Name the blood parasite species.
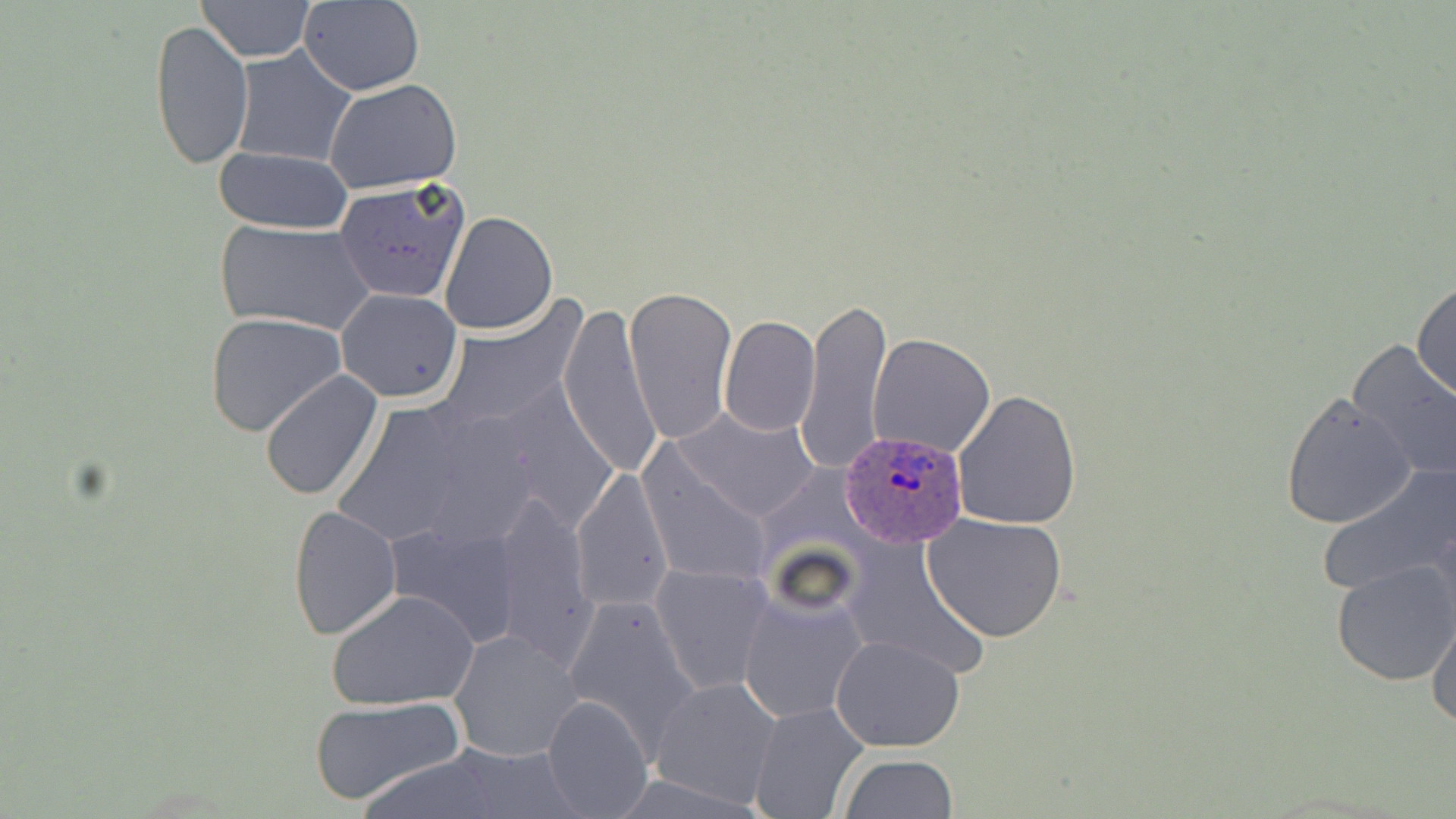

Plasmodium ovale.

Summary:
  - Coordinate format: approximate bounding boxes as named x1/y1/x2/y2 corners in pixels
  - Uninfected red blood cell locations: (x1=195, y1=0, x2=315, y2=61), (x1=298, y1=0, x2=423, y2=95), (x1=150, y1=18, x2=253, y2=171), (x1=231, y1=47, x2=357, y2=167), (x1=323, y1=78, x2=462, y2=194), (x1=210, y1=147, x2=355, y2=234), (x1=336, y1=178, x2=470, y2=303), (x1=439, y1=211, x2=559, y2=335), (x1=213, y1=219, x2=379, y2=335), (x1=1412, y1=278, x2=1455, y2=405), (x1=624, y1=286, x2=737, y2=446), (x1=336, y1=288, x2=464, y2=402), (x1=798, y1=293, x2=892, y2=474), (x1=434, y1=296, x2=587, y2=435), (x1=559, y1=303, x2=661, y2=479), (x1=205, y1=312, x2=347, y2=436), (x1=719, y1=316, x2=821, y2=436), (x1=868, y1=333, x2=995, y2=458), (x1=1344, y1=336, x2=1456, y2=485), (x1=260, y1=368, x2=384, y2=501), (x1=951, y1=387, x2=1081, y2=531), (x1=1280, y1=392, x2=1415, y2=529), (x1=674, y1=409, x2=823, y2=523), (x1=638, y1=450, x2=773, y2=587), (x1=1316, y1=461, x2=1456, y2=599), (x1=571, y1=467, x2=674, y2=613), (x1=488, y1=491, x2=600, y2=668), (x1=287, y1=506, x2=403, y2=640), (x1=922, y1=513, x2=1069, y2=643), (x1=844, y1=538, x2=989, y2=677), (x1=1330, y1=559, x2=1456, y2=685), (x1=652, y1=564, x2=774, y2=694), (x1=327, y1=588, x2=479, y2=710), (x1=737, y1=588, x2=868, y2=723), (x1=562, y1=594, x2=701, y2=748), (x1=1426, y1=608, x2=1456, y2=731), (x1=449, y1=630, x2=583, y2=762), (x1=830, y1=636, x2=967, y2=752), (x1=649, y1=677, x2=783, y2=807), (x1=542, y1=694, x2=652, y2=819), (x1=308, y1=696, x2=466, y2=807), (x1=750, y1=702, x2=870, y2=819), (x1=438, y1=742, x2=583, y2=818), (x1=357, y1=753, x2=507, y2=818), (x1=840, y1=755, x2=959, y2=818)
  - Plasmodium ovale-infected red blood cell locations: (x1=840, y1=432, x2=970, y2=547)
  - Image size: 1456×819 pixels
  - Field of view: one of a larger specimen
  - Modality: light microscopy
  - Magnification: 1000x
  - Stain: May-Grünwald-Giemsa
  - Preparation: thin blood smear